Outline each blood parasite and name the species.
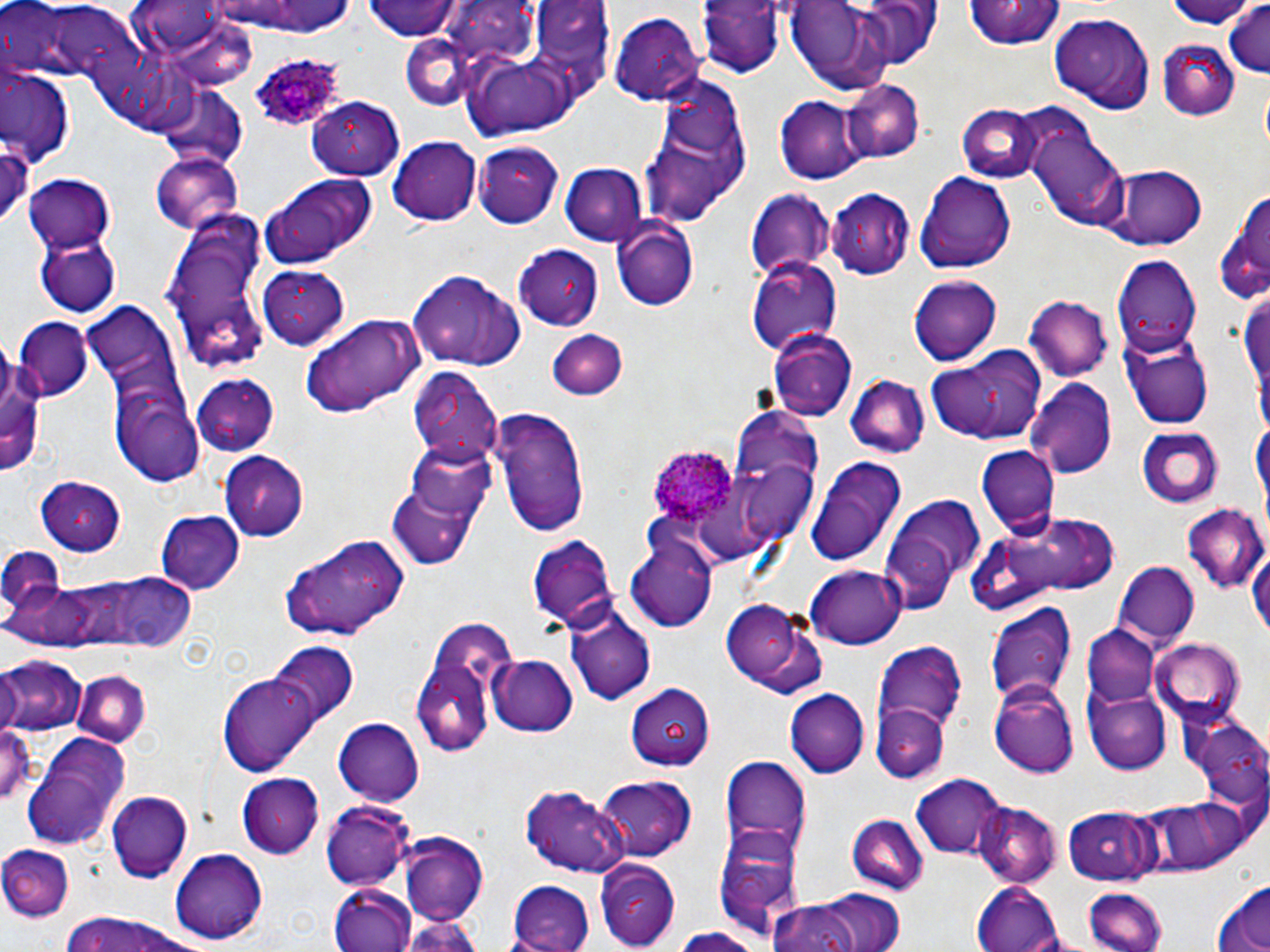

Approximate bounding boxes as [x1, y1, x2, y2] in pixels.
Plasmodium ovale-infected red blood cells: [249, 52, 360, 142], [649, 446, 738, 529].
No Plasmodium falciparum, Plasmodium malariae, Plasmodium vivax, Babesia divergens, or Trypanosoma brucei observed.

Uninfected red blood cell locations: [360, 0, 464, 41], [1166, 0, 1258, 30], [696, 1, 781, 77], [781, 1, 901, 93], [855, 1, 940, 69], [200, 2, 364, 38], [964, 2, 1062, 52], [11, 4, 137, 84], [1222, 4, 1269, 81], [425, 5, 614, 140], [610, 13, 704, 104], [1050, 13, 1156, 113], [400, 32, 483, 109], [1157, 38, 1239, 118], [1, 66, 74, 165], [640, 73, 752, 227], [841, 79, 922, 163], [156, 83, 248, 167], [774, 94, 868, 183], [307, 97, 421, 185], [957, 104, 1045, 183], [1021, 111, 1129, 229], [388, 135, 482, 225], [0, 136, 33, 231], [476, 141, 563, 228], [152, 152, 243, 236], [560, 162, 647, 244], [1097, 166, 1208, 251], [259, 172, 375, 268], [915, 172, 1017, 273], [24, 174, 118, 251], [827, 187, 915, 278], [1214, 188, 1269, 306], [745, 190, 835, 282], [166, 215, 273, 377], [612, 221, 700, 311], [35, 233, 118, 317], [515, 246, 606, 328], [1111, 256, 1203, 358], [746, 257, 842, 354], [260, 266, 350, 351], [410, 271, 525, 372], [908, 274, 1003, 364], [1238, 285, 1269, 428], [1025, 295, 1112, 381], [81, 300, 186, 411], [301, 315, 422, 417], [14, 318, 93, 400], [1122, 329, 1214, 430], [770, 330, 857, 421], [546, 331, 627, 401], [0, 338, 42, 481], [928, 349, 1044, 447], [407, 367, 503, 468], [192, 372, 278, 456], [111, 374, 204, 482], [844, 376, 928, 459], [1029, 378, 1119, 476], [490, 404, 592, 539], [731, 408, 821, 522], [1137, 425, 1223, 509], [403, 437, 499, 530], [977, 446, 1057, 537], [219, 453, 307, 541], [806, 456, 907, 565], [388, 471, 484, 569], [37, 478, 128, 553], [879, 493, 985, 612], [1183, 504, 1267, 594], [154, 511, 243, 595], [981, 512, 1126, 609], [626, 529, 719, 634], [528, 531, 618, 633], [278, 532, 409, 642], [1248, 545, 1270, 646], [0, 547, 66, 619], [1116, 561, 1200, 647], [807, 565, 905, 648], [102, 572, 201, 653], [719, 598, 823, 697], [564, 600, 656, 706], [983, 603, 1077, 712], [413, 620, 517, 761], [1085, 624, 1161, 706], [1150, 636, 1245, 723], [268, 643, 356, 728], [876, 643, 967, 734], [488, 653, 576, 735], [2, 656, 84, 735], [75, 668, 150, 748], [221, 673, 321, 777], [989, 683, 1079, 776], [629, 684, 716, 768], [1087, 685, 1171, 773], [785, 688, 871, 777], [872, 702, 949, 783], [1178, 707, 1269, 809], [332, 718, 425, 804], [0, 721, 35, 811], [21, 734, 131, 850], [720, 755, 811, 854], [238, 772, 324, 858], [907, 773, 1009, 861], [594, 775, 694, 862], [524, 785, 628, 878], [107, 791, 193, 882], [1152, 795, 1251, 874], [323, 799, 416, 891], [974, 802, 1061, 886], [1063, 804, 1162, 885], [845, 812, 927, 892], [713, 826, 803, 939], [399, 834, 488, 924], [2, 843, 74, 920], [171, 848, 267, 942], [596, 859, 680, 948], [507, 881, 596, 952], [972, 881, 1064, 951], [1211, 881, 1270, 951], [327, 885, 417, 952], [1079, 885, 1167, 951], [814, 887, 906, 952], [765, 898, 868, 952], [59, 913, 208, 952], [400, 914, 479, 952], [668, 927, 758, 952]. Slide-level diagnosis: Plasmodium ovale. Thin blood smear. Captured at 1000x magnification. May-Grünwald-Giemsa stain. Image is 1270×952 pixels. Single field of view. Optical microscopy.